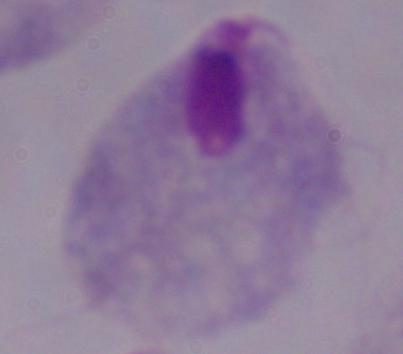
modality = micrograph
identification = trichomonad
magnification = 1000x